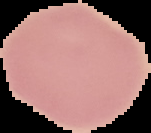

From a thin blood smear. Image is 151×133 pixels. Malaria status: uninfected. Cell region segmented out of the field of view; the surrounding area is masked to black.